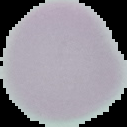
Image is 127×127 pixels. Result: no Plasmodium parasites seen. Segmented cell region on a black background. From a thin blood smear.